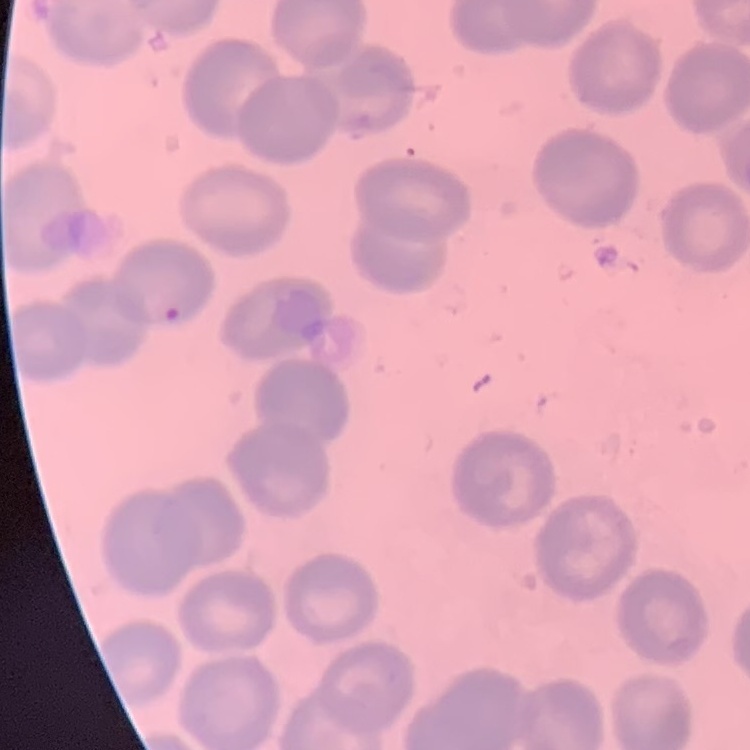

Summary:
  - Erythrocyte morphology: no rouleaux formation
  - Image type: one tile cut from a larger photomicrograph
  - Stain: Field's or Giemsa
  - Preparation: thin peripheral smear